Outline each uninfected red blood cell.
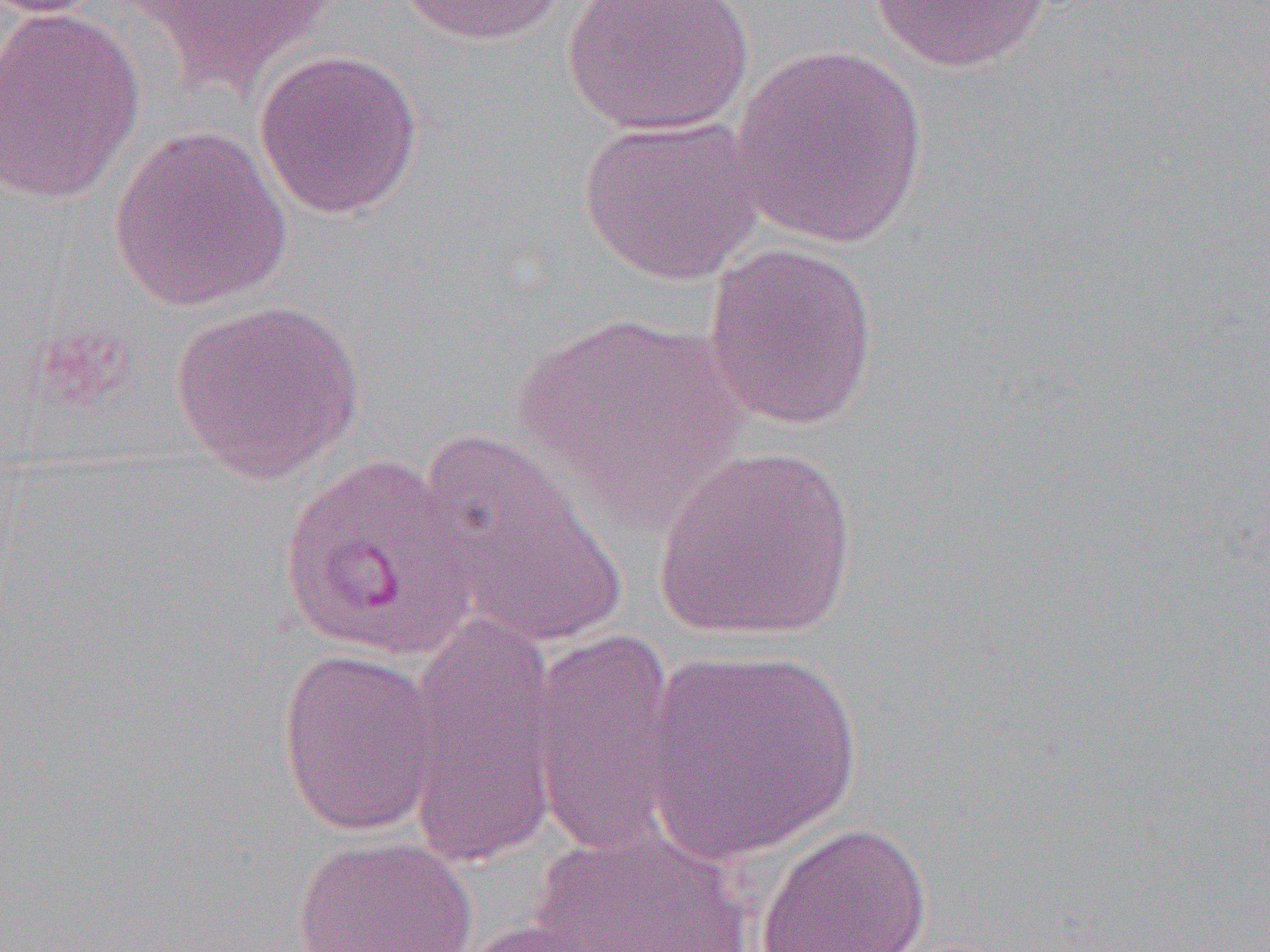

Approximate bounding boxes as named x1/y1/x2/y2 corners in pixels.
Uninfected red blood cells: (x1=123, y1=0, x2=342, y2=98), (x1=396, y1=0, x2=574, y2=47), (x1=562, y1=0, x2=755, y2=137), (x1=869, y1=0, x2=1052, y2=73), (x1=0, y1=5, x2=145, y2=205), (x1=730, y1=43, x2=932, y2=247), (x1=253, y1=48, x2=424, y2=218), (x1=577, y1=116, x2=766, y2=285), (x1=108, y1=123, x2=293, y2=312), (x1=702, y1=242, x2=880, y2=430), (x1=169, y1=298, x2=364, y2=483), (x1=513, y1=312, x2=749, y2=519), (x1=418, y1=433, x2=626, y2=646), (x1=653, y1=446, x2=858, y2=644), (x1=403, y1=613, x2=562, y2=869), (x1=527, y1=629, x2=684, y2=858), (x1=276, y1=647, x2=444, y2=837), (x1=641, y1=647, x2=863, y2=863), (x1=755, y1=820, x2=932, y2=952), (x1=527, y1=825, x2=757, y2=952), (x1=292, y1=835, x2=479, y2=952), (x1=460, y1=916, x2=627, y2=951).

Summary:
  - Slide-level diagnosis: Plasmodium vivax
  - Magnification: 1000x
  - Preparation: thin blood film
  - Image size: 1270×952 pixels
  - Modality: light microscopy
  - Field of view: one of a larger specimen